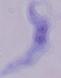
modality = photomicrograph
identification = trypanosome
magnification = 1000x